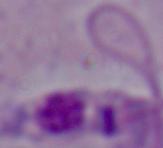
{
  "magnification": "1000x",
  "modality": "micrograph",
  "identification": "Leishmania"
}